Assess this cell for malaria.
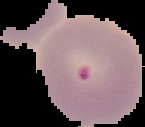

Parasitized.

image_type: segmented cell region on a black background
image_size: 145×127 pixels
preparation: thin blood smear